State which parasite is depicted.
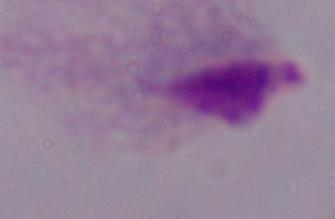

A trichomonad.

Summary:
  - Magnification: 1000x
  - Modality: photomicrograph